Locate every leukocyte (white blood cell).
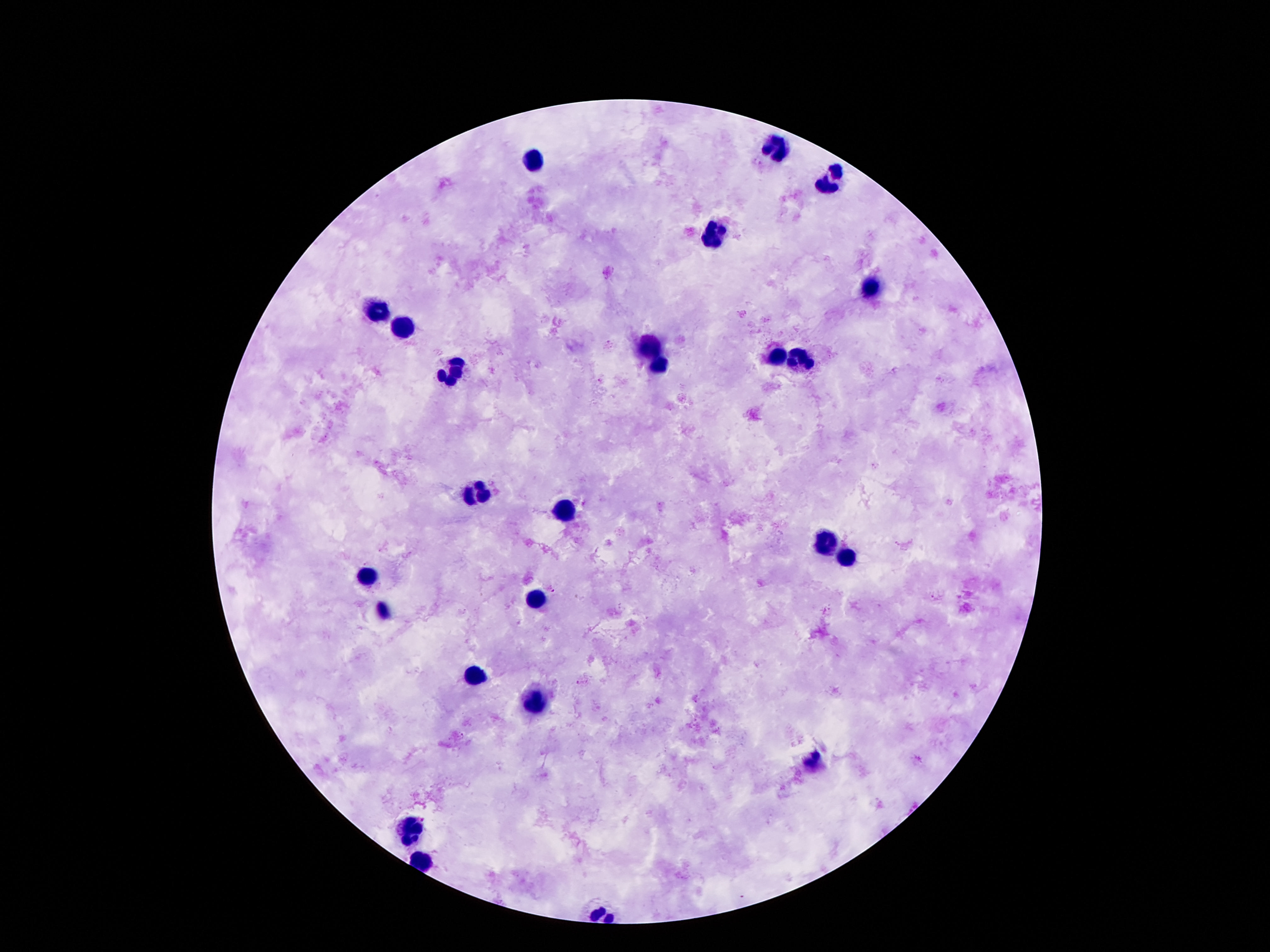
Approximate centers as {x, y} in pixels.
Leukocytes: {773, 144}, {535, 163}, {828, 180}, {713, 236}, {873, 294}, {376, 312}, {404, 328}, {654, 347}, {779, 357}, {803, 363}, {658, 366}, {455, 372}, {478, 491}, {564, 514}, {828, 544}, {846, 554}, {363, 578}, {536, 601}, {381, 610}, {473, 677}, {534, 706}, {811, 762}, {415, 834}.

{
  "patient_malaria_status": "uninfected",
  "capture": "smartphone camera through the microscope eyepiece",
  "field_of_view": "single",
  "preparation": "thick peripheral-blood smear",
  "magnification": "100x",
  "image_size": "1270×952 pixels",
  "stain": "Giemsa"
}